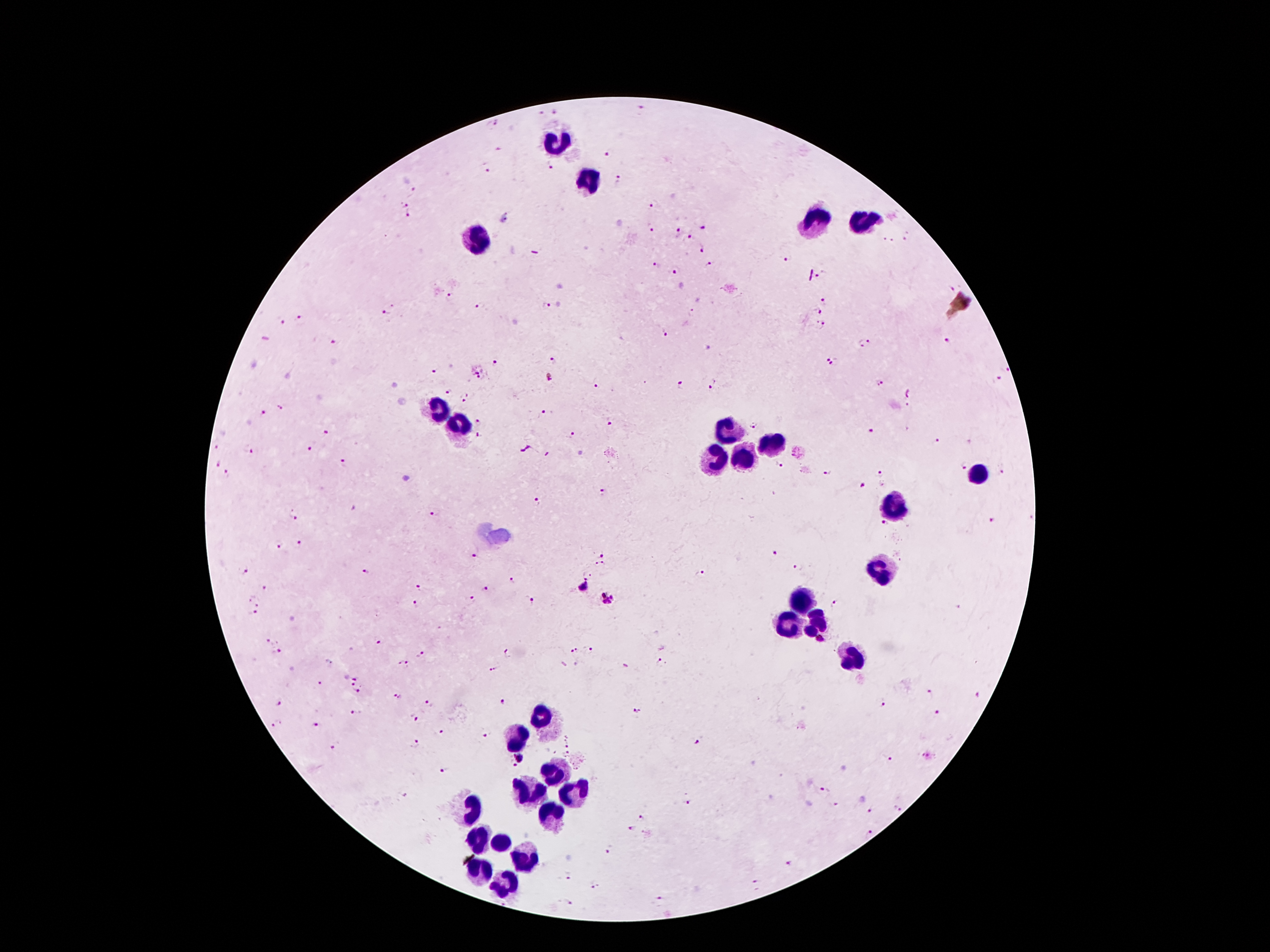

Approximate object centers, in pixels from the top-left corner.
Summary:
  - Malaria parasite locations (subset; some too small to resolve): (x=643, y=109), (x=556, y=110), (x=541, y=114), (x=494, y=123), (x=608, y=153), (x=549, y=166), (x=487, y=169), (x=619, y=179), (x=413, y=190), (x=652, y=205), (x=403, y=206), (x=408, y=216), (x=705, y=227), (x=651, y=230), (x=679, y=231), (x=691, y=236), (x=532, y=237), (x=907, y=237), (x=890, y=241), (x=703, y=249), (x=788, y=258), (x=657, y=263), (x=709, y=264), (x=676, y=272), (x=819, y=277), (x=949, y=289), (x=451, y=297), (x=825, y=302), (x=481, y=306), (x=547, y=306), (x=819, y=310), (x=385, y=312), (x=693, y=312), (x=301, y=318), (x=280, y=322), (x=821, y=326), (x=665, y=334), (x=946, y=342), (x=334, y=343), (x=865, y=343), (x=553, y=361), (x=496, y=362), (x=833, y=362), (x=479, y=369), (x=433, y=370), (x=1007, y=370), (x=551, y=377), (x=998, y=378), (x=597, y=383), (x=713, y=384), (x=879, y=384), (x=681, y=386), (x=450, y=391), (x=910, y=392), (x=466, y=397), (x=282, y=407), (x=545, y=412), (x=263, y=414), (x=481, y=418), (x=609, y=423), (x=755, y=426), (x=871, y=431), (x=325, y=432), (x=572, y=435), (x=478, y=436), (x=937, y=442), (x=217, y=447), (x=310, y=448), (x=249, y=451), (x=344, y=463), (x=781, y=464), (x=217, y=465), (x=963, y=467), (x=829, y=471), (x=1002, y=472), (x=226, y=475), (x=878, y=475), (x=862, y=486), (x=605, y=493), (x=536, y=501), (x=294, y=515), (x=432, y=515), (x=991, y=520), (x=885, y=523), (x=298, y=544), (x=279, y=545), (x=773, y=551), (x=604, y=553), (x=475, y=555), (x=600, y=565), (x=797, y=566), (x=243, y=571), (x=368, y=571), (x=702, y=574), (x=514, y=580), (x=265, y=586), (x=418, y=587), (x=584, y=587), (x=486, y=590), (x=606, y=598), (x=531, y=599), (x=254, y=600), (x=470, y=600), (x=416, y=605), (x=834, y=606), (x=253, y=613), (x=820, y=640), (x=268, y=642), (x=378, y=643), (x=591, y=650), (x=573, y=651), (x=277, y=653), (x=419, y=653), (x=505, y=655), (x=403, y=662), (x=662, y=662), (x=625, y=665), (x=493, y=669), (x=350, y=678), (x=321, y=684), (x=356, y=692), (x=931, y=695), (x=398, y=696), (x=979, y=696), (x=506, y=699), (x=428, y=703), (x=279, y=704), (x=882, y=704), (x=635, y=709), (x=357, y=712), (x=937, y=714), (x=414, y=717), (x=276, y=724), (x=319, y=724), (x=440, y=729), (x=488, y=735), (x=567, y=741), (x=696, y=741), (x=415, y=744), (x=332, y=748), (x=567, y=753), (x=520, y=757), (x=888, y=763), (x=514, y=765), (x=444, y=770), (x=825, y=791), (x=687, y=801), (x=896, y=807), (x=868, y=813), (x=641, y=817), (x=631, y=830), (x=869, y=833), (x=608, y=848), (x=790, y=864), (x=568, y=874), (x=595, y=884), (x=755, y=884), (x=568, y=901), (x=660, y=901)
  - Leukocyte locations: (x=557, y=140), (x=585, y=184), (x=860, y=223), (x=815, y=224), (x=482, y=240), (x=440, y=410), (x=460, y=428), (x=727, y=432), (x=771, y=441), (x=714, y=454), (x=745, y=459), (x=976, y=472), (x=895, y=505), (x=882, y=571), (x=806, y=599), (x=815, y=623), (x=784, y=626), (x=855, y=658), (x=544, y=718), (x=517, y=741), (x=555, y=774), (x=528, y=795), (x=572, y=795), (x=469, y=808), (x=555, y=812), (x=479, y=836), (x=502, y=845), (x=526, y=857), (x=486, y=872), (x=508, y=883)
  - Image size: 1270×952 pixels
  - Capture: smartphone through the microscope eyepiece
  - Patient malaria status: positive for Plasmodium falciparum
  - Stain: Giemsa
  - Field of view: single
  - Preparation: thick blood smear
  - Magnification: 100x